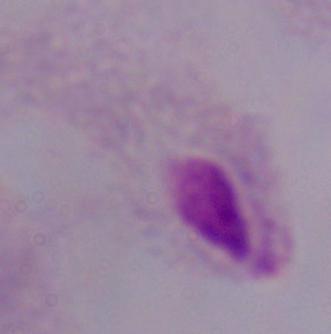 Captured at 1000x magnification. A trichomonad is shown. Micrograph.